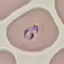

Summary:
  - Result: malaria parasites detected
  - Stain: Giemsa
  - Image type: cell patch, automatically extracted from a larger field of view and resized to 64 × 64 pixels
  - Capture: smartphone through the microscope eyepiece
  - Preparation: thin smear